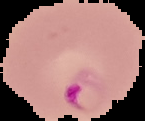

Summary:
  - Preparation: thin blood film
  - Image type: segmented cell region with the area outside set to black
  - Image size: 145×121 pixels
  - Result: Plasmodium parasites detected